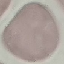
Summary:
  - Result: no malaria parasites detected
  - Image type: automatically extracted cell patch, resized to 64 × 64 pixels
  - Preparation: thin blood film
  - Stain: Giemsa
  - Capture: smartphone through the microscope eyepiece